State which parasite is depicted.
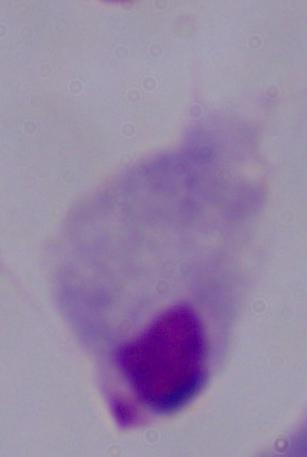

A trichomonad.

Summary:
  - Magnification: 1000x
  - Modality: micrograph